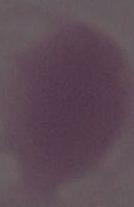 Photomicrograph. 1000x magnification. An erythrocyte is seen.